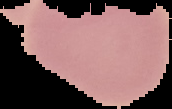
Summary:
  - Image size: 172×109 pixels
  - Preparation: thin blood film
  - Image type: segmented cell region on a black background
  - Malaria status: parasitized